Evaluate for Plasmodium parasites.
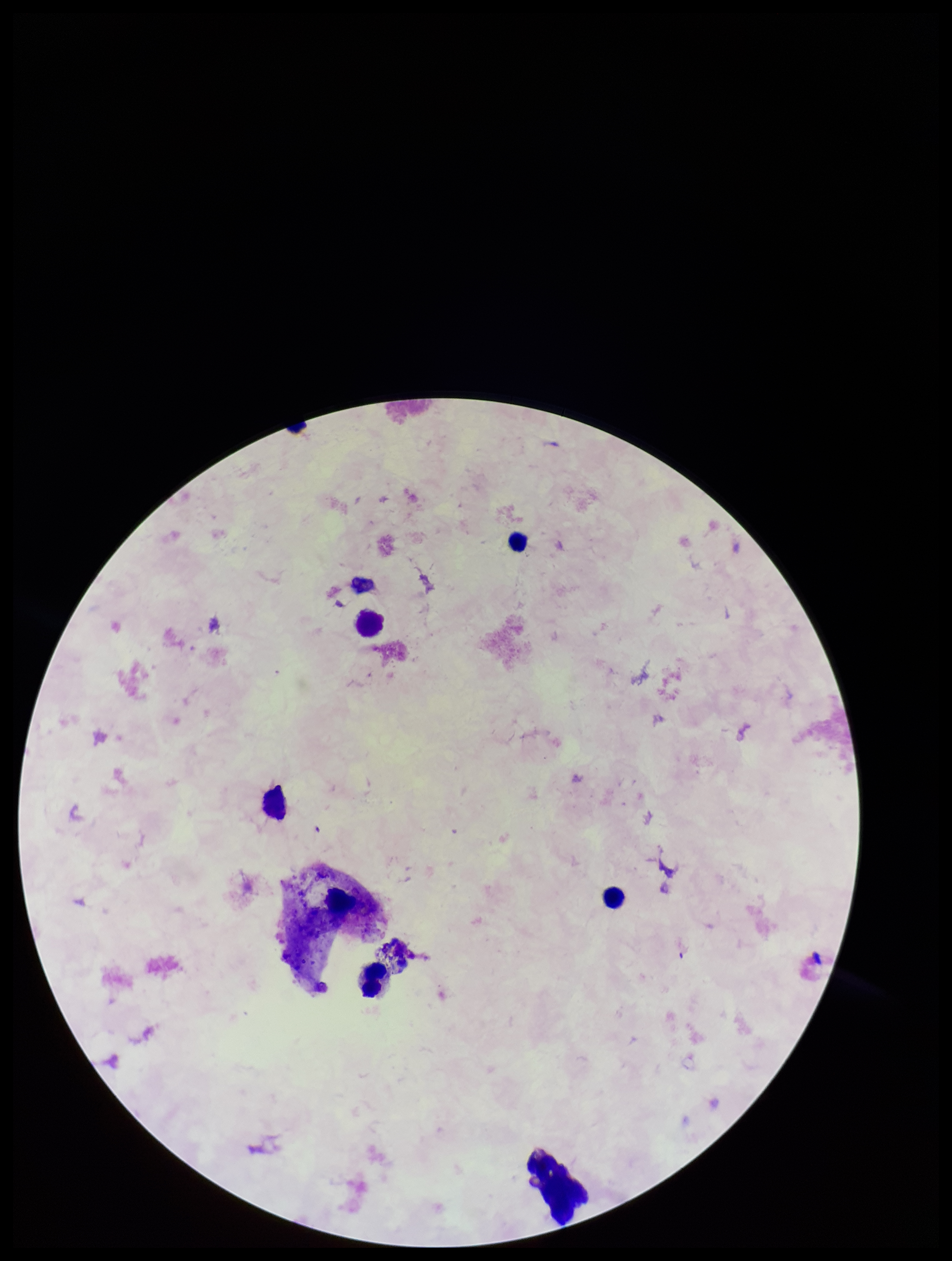

None seen.

Summary:
  - Preparation: thick smear
  - Stain: Giemsa
  - Capture: smartphone photograph through the microscope eyepiece
  - Field of view: single
  - Leukocyte count: 5
  - Parasite count: 0
  - Image size: 952×1261 pixels
  - Patient malaria status: negative